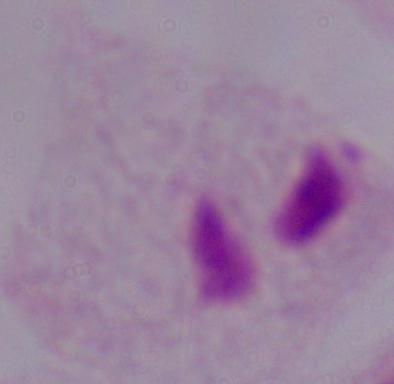
modality = photomicrograph
identification = trichomonad
magnification = 1000x